Identify the parasite.
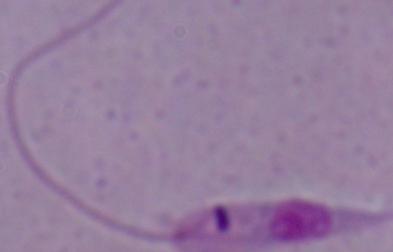
This is Leishmania.

magnification = 1000x
modality = micrograph